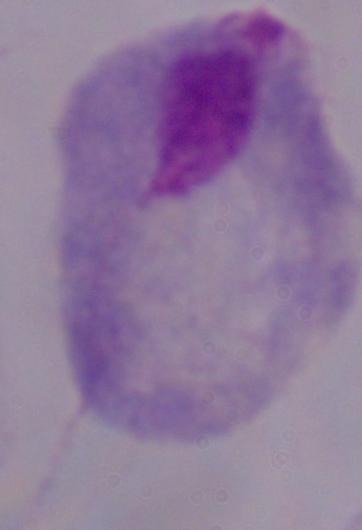
magnification = 1000x
identification = trichomonad
modality = micrograph